Point out each Plasmodium parasite.
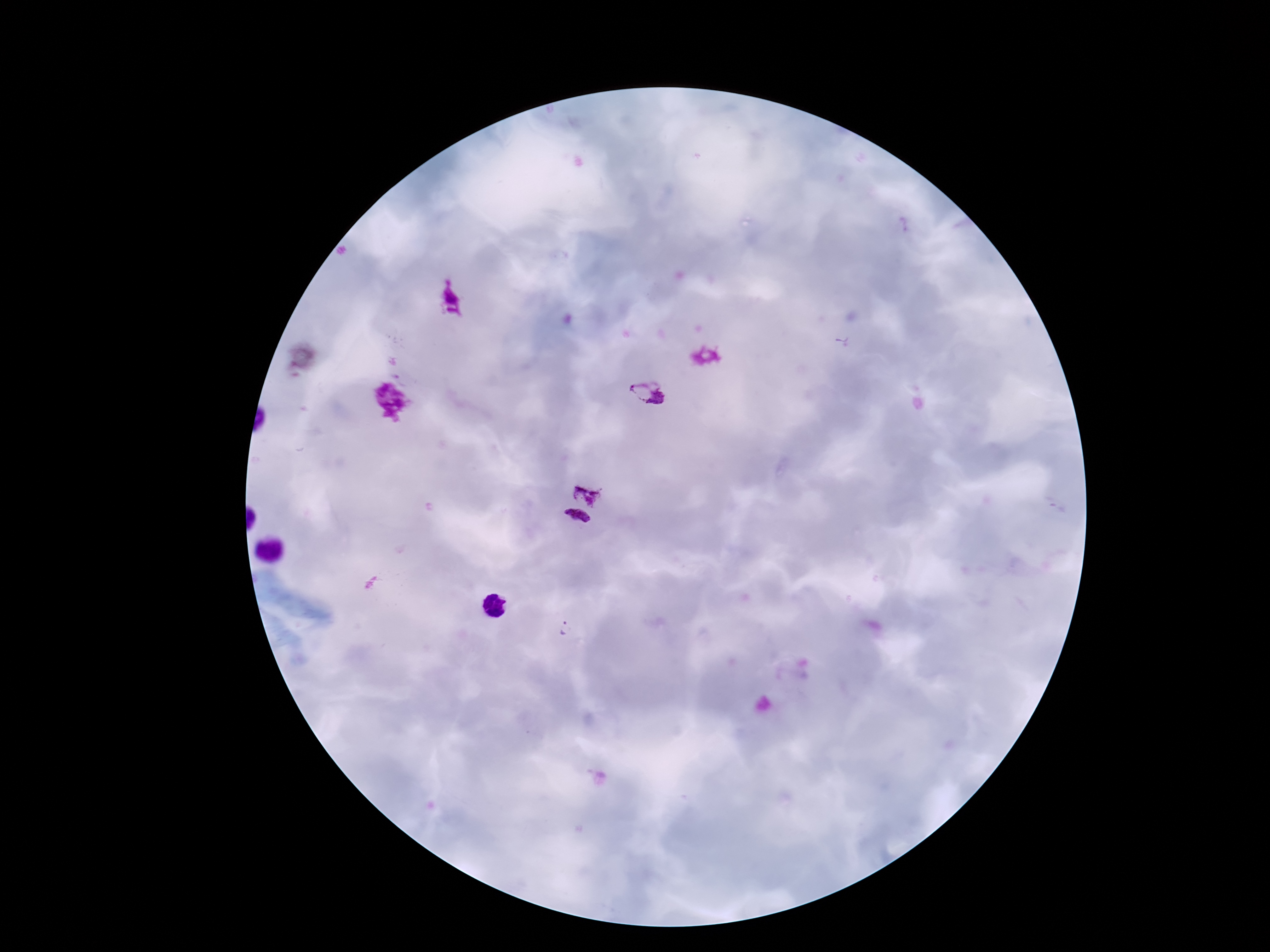

Approximate object centers, in pixels from the top-left corner.
Plasmodium parasites: (x=646, y=392), (x=586, y=489), (x=575, y=522), (x=566, y=628).

Patient malaria status: positive. Image is 1270×952 pixels. Single field of view. Smartphone photograph taken through the microscope eyepiece. Giemsa stain. Thick blood film. 100x magnification.